Locate every uninfected red blood cell.
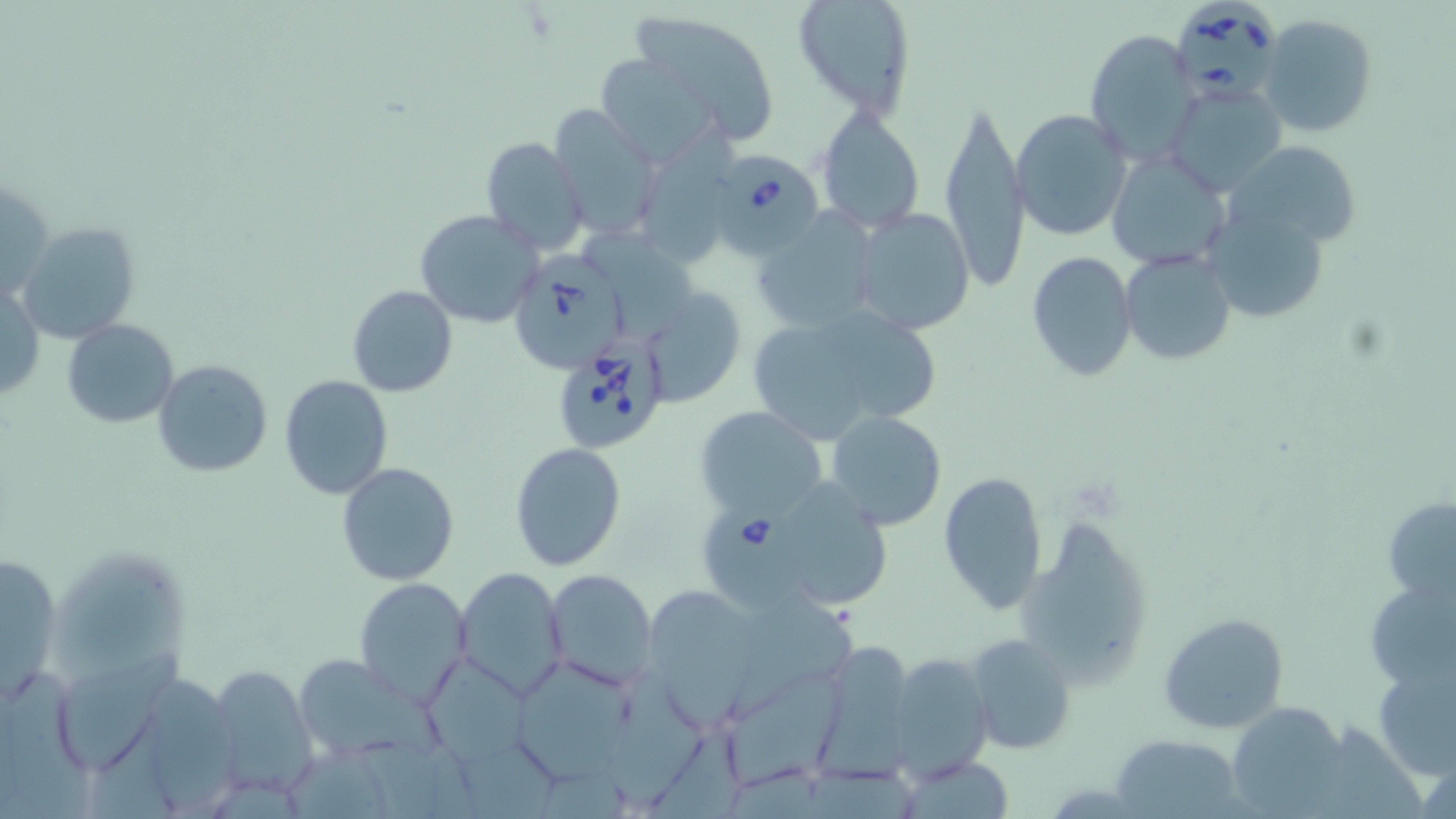

Approximate bounding boxes as (x1,y1)-(x2,y2) corner pairs in pixels.
Uninfected red blood cells: (791,0)-(917,118), (626,7)-(780,143), (1259,13)-(1378,137), (1083,29)-(1201,159), (593,52)-(730,168), (1168,81)-(1286,197), (940,96)-(1030,295), (551,105)-(661,238), (813,105)-(926,233), (1011,109)-(1132,240), (639,121)-(739,260), (481,137)-(589,256), (1228,147)-(1367,249), (1106,149)-(1234,272), (849,207)-(976,336), (752,209)-(880,337), (414,210)-(543,329), (1215,213)-(1333,328), (17,220)-(142,345), (587,222)-(697,343), (1119,250)-(1236,366), (1025,251)-(1138,380), (1,279)-(45,406), (348,284)-(457,397), (645,285)-(746,405), (745,303)-(938,446), (63,319)-(180,429), (104,343)-(231,478), (151,359)-(273,478), (279,376)-(393,498), (694,406)-(829,523), (825,410)-(948,530), (510,442)-(628,572), (336,461)-(460,587), (937,471)-(1047,612), (794,484)-(896,607), (1383,496)-(1456,604), (1015,512)-(1155,689), (0,550)-(65,701), (56,558)-(201,676), (453,567)-(569,701), (544,568)-(657,690), (1364,575)-(1456,694), (354,577)-(474,704), (652,587)-(755,740), (723,592)-(865,716), (1160,613)-(1287,734), (965,633)-(1077,755), (826,643)-(920,783), (64,646)-(194,767), (884,651)-(993,778), (290,654)-(447,766), (430,658)-(550,772), (508,658)-(636,784), (1374,662)-(1455,780), (208,664)-(319,797), (0,665)-(98,819), (728,667)-(851,795), (151,678)-(248,811), (607,678)-(709,808), (1227,703)-(1347,815), (1111,733)-(1245,818), (895,757)-(1017,816).

babesia_divergens_infected_red_blood_cell_locations: 'approximate bounding boxes as (x1,y1)-(x2,y2) corner pairs in pixels: (1171,2)-(1280,103), (723,158)-(830,252), (507,253)-(629,373), (552,337)-(671,454), (702,503)-(830,609)'
slide_level_diagnosis: Babesia divergens
field_of_view: single
preparation: thin blood film
image_size: 1456×819 pixels
modality: optical microscopy
magnification: 1000x
stain: May-Grünwald-Giemsa